Assess this cell for malaria.
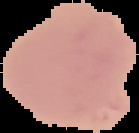

Uninfected.

Image is 139×133 pixels. From a thin blood film. Cell region segmented out of the field of view; the surrounding area is masked to black.